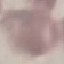
Summary:
  - Malaria status: uninfected
  - Image type: automatically extracted cell patch, resized to 64 × 64 pixels
  - Capture: smartphone through the microscope eyepiece
  - Preparation: thin blood film
  - Stain: Giemsa